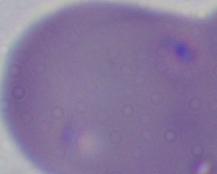

magnification = 1000x
identification = Babesia
modality = photomicrograph